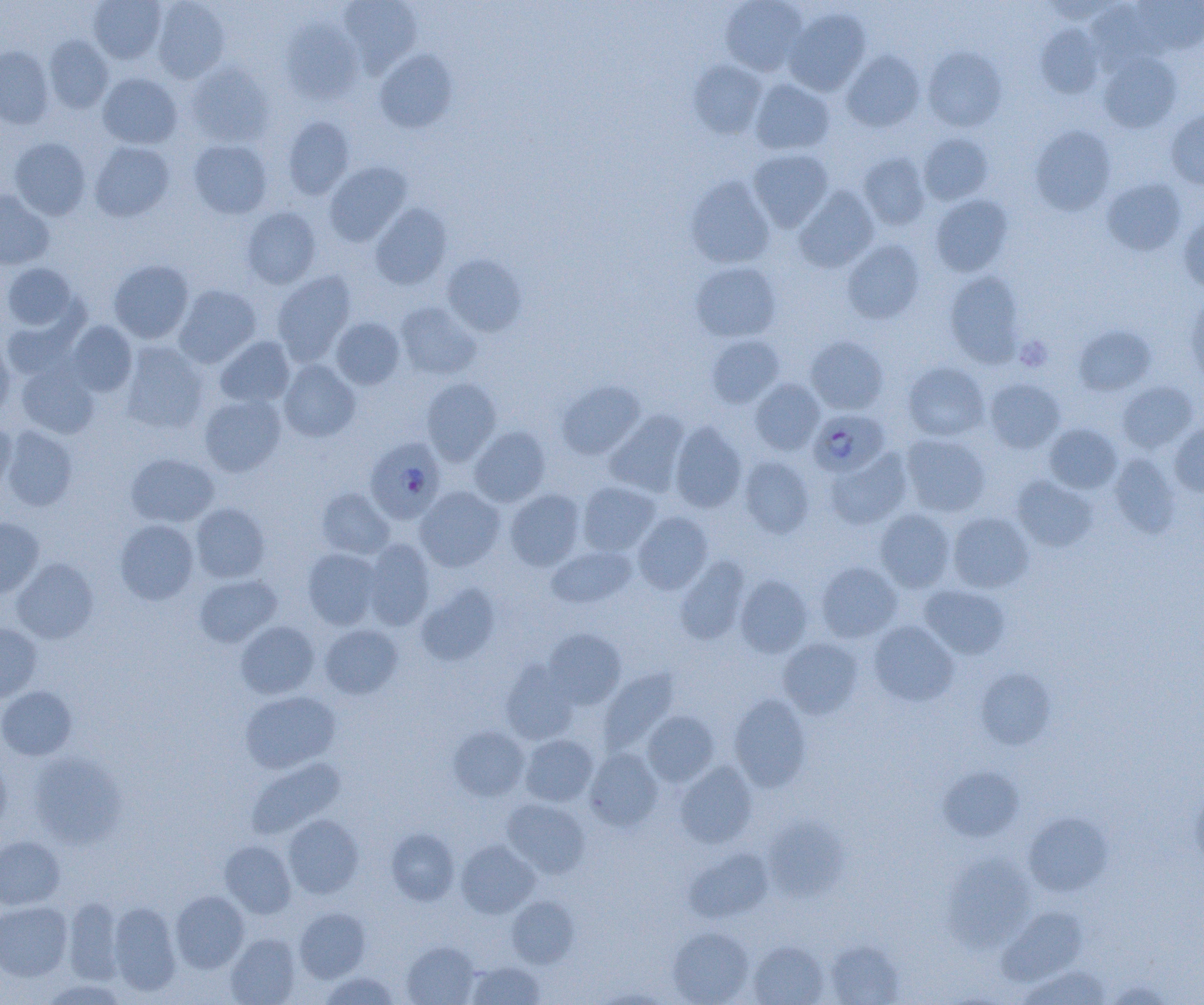 Approximate bounding boxes as named x1/y1/x2/y2 corners in pixels. Platelet locations: (x1=1016, y1=336, x2=1052, y2=371). Uninfected red blood cell locations: (x1=89, y1=0, x2=166, y2=63), (x1=151, y1=0, x2=230, y2=83), (x1=339, y1=0, x2=422, y2=77), (x1=720, y1=0, x2=807, y2=76), (x1=1133, y1=0, x2=1204, y2=55), (x1=1086, y1=2, x2=1162, y2=69), (x1=784, y1=7, x2=870, y2=96), (x1=281, y1=20, x2=363, y2=104), (x1=1036, y1=23, x2=1104, y2=99), (x1=44, y1=36, x2=113, y2=113), (x1=0, y1=46, x2=54, y2=129), (x1=923, y1=46, x2=1007, y2=131), (x1=374, y1=50, x2=458, y2=134), (x1=841, y1=50, x2=925, y2=132), (x1=1099, y1=52, x2=1182, y2=132), (x1=688, y1=59, x2=767, y2=138), (x1=185, y1=62, x2=274, y2=147), (x1=98, y1=72, x2=182, y2=148), (x1=749, y1=78, x2=834, y2=155), (x1=1166, y1=109, x2=1204, y2=190), (x1=282, y1=116, x2=354, y2=199), (x1=1030, y1=125, x2=1116, y2=215), (x1=919, y1=133, x2=994, y2=205), (x1=9, y1=137, x2=91, y2=220), (x1=188, y1=139, x2=273, y2=218), (x1=90, y1=141, x2=174, y2=221), (x1=747, y1=148, x2=834, y2=231), (x1=858, y1=152, x2=930, y2=230), (x1=324, y1=161, x2=412, y2=246), (x1=686, y1=175, x2=775, y2=268), (x1=1102, y1=178, x2=1186, y2=256), (x1=794, y1=186, x2=878, y2=272), (x1=0, y1=190, x2=54, y2=269), (x1=930, y1=194, x2=1013, y2=277), (x1=370, y1=203, x2=451, y2=290), (x1=241, y1=207, x2=321, y2=288), (x1=1178, y1=211, x2=1204, y2=294), (x1=842, y1=239, x2=924, y2=324), (x1=441, y1=254, x2=527, y2=336), (x1=109, y1=259, x2=194, y2=343), (x1=691, y1=261, x2=782, y2=342), (x1=2, y1=262, x2=78, y2=331), (x1=272, y1=270, x2=357, y2=364), (x1=944, y1=271, x2=1025, y2=366), (x1=174, y1=284, x2=261, y2=367), (x1=1184, y1=293, x2=1204, y2=385), (x1=396, y1=301, x2=481, y2=380), (x1=2, y1=308, x2=85, y2=383), (x1=330, y1=317, x2=405, y2=389), (x1=67, y1=320, x2=138, y2=396), (x1=1074, y1=324, x2=1155, y2=396), (x1=706, y1=334, x2=785, y2=408), (x1=805, y1=335, x2=889, y2=414), (x1=215, y1=336, x2=296, y2=408), (x1=0, y1=338, x2=15, y2=419), (x1=120, y1=341, x2=208, y2=434), (x1=278, y1=360, x2=360, y2=442), (x1=903, y1=361, x2=989, y2=442), (x1=16, y1=362, x2=99, y2=439), (x1=421, y1=377, x2=501, y2=465), (x1=984, y1=378, x2=1065, y2=453), (x1=749, y1=379, x2=825, y2=455), (x1=558, y1=380, x2=645, y2=460), (x1=1117, y1=381, x2=1198, y2=453), (x1=198, y1=393, x2=286, y2=477), (x1=604, y1=411, x2=690, y2=497), (x1=0, y1=419, x2=16, y2=493), (x1=669, y1=422, x2=747, y2=513), (x1=1169, y1=422, x2=1204, y2=496), (x1=1044, y1=423, x2=1122, y2=493), (x1=2, y1=426, x2=78, y2=511), (x1=469, y1=426, x2=550, y2=507), (x1=901, y1=434, x2=990, y2=517), (x1=825, y1=448, x2=912, y2=529), (x1=126, y1=453, x2=219, y2=528), (x1=1109, y1=453, x2=1180, y2=537), (x1=739, y1=456, x2=815, y2=538), (x1=1011, y1=475, x2=1097, y2=551), (x1=577, y1=481, x2=660, y2=555), (x1=415, y1=486, x2=505, y2=572), (x1=316, y1=487, x2=394, y2=559), (x1=505, y1=489, x2=585, y2=571), (x1=190, y1=502, x2=270, y2=583), (x1=875, y1=509, x2=956, y2=592), (x1=633, y1=511, x2=713, y2=594), (x1=948, y1=512, x2=1033, y2=593), (x1=0, y1=518, x2=44, y2=597), (x1=115, y1=519, x2=199, y2=604), (x1=363, y1=539, x2=435, y2=630), (x1=546, y1=544, x2=637, y2=608), (x1=303, y1=548, x2=382, y2=629), (x1=675, y1=556, x2=750, y2=645), (x1=11, y1=558, x2=98, y2=643), (x1=816, y1=562, x2=902, y2=643), (x1=195, y1=574, x2=281, y2=647), (x1=735, y1=574, x2=812, y2=657), (x1=416, y1=582, x2=500, y2=666), (x1=919, y1=584, x2=1011, y2=659), (x1=868, y1=620, x2=959, y2=706), (x1=236, y1=621, x2=320, y2=699), (x1=0, y1=623, x2=42, y2=702), (x1=320, y1=624, x2=402, y2=699), (x1=543, y1=629, x2=626, y2=709), (x1=778, y1=638, x2=863, y2=718), (x1=501, y1=660, x2=578, y2=744), (x1=599, y1=667, x2=680, y2=754), (x1=975, y1=667, x2=1055, y2=749), (x1=0, y1=685, x2=77, y2=760), (x1=240, y1=691, x2=340, y2=774), (x1=729, y1=694, x2=811, y2=791), (x1=642, y1=710, x2=720, y2=787), (x1=448, y1=725, x2=530, y2=801), (x1=520, y1=734, x2=598, y2=806), (x1=584, y1=749, x2=663, y2=830), (x1=28, y1=752, x2=127, y2=847), (x1=0, y1=753, x2=12, y2=834), (x1=246, y1=757, x2=345, y2=839), (x1=675, y1=762, x2=757, y2=848), (x1=938, y1=766, x2=1024, y2=842), (x1=1191, y1=786, x2=1204, y2=869), (x1=502, y1=799, x2=590, y2=878), (x1=1023, y1=812, x2=1113, y2=896), (x1=282, y1=814, x2=363, y2=898), (x1=763, y1=818, x2=847, y2=900), (x1=386, y1=828, x2=460, y2=906), (x1=0, y1=836, x2=65, y2=910), (x1=220, y1=840, x2=296, y2=918), (x1=456, y1=840, x2=540, y2=917), (x1=684, y1=847, x2=773, y2=922), (x1=943, y1=853, x2=1035, y2=950), (x1=171, y1=890, x2=249, y2=973), (x1=507, y1=896, x2=579, y2=968), (x1=64, y1=897, x2=126, y2=984), (x1=0, y1=900, x2=73, y2=981), (x1=108, y1=902, x2=181, y2=996), (x1=294, y1=907, x2=370, y2=982), (x1=999, y1=907, x2=1087, y2=985), (x1=667, y1=926, x2=753, y2=1005), (x1=225, y1=933, x2=300, y2=1005), (x1=401, y1=940, x2=480, y2=1005), (x1=825, y1=940, x2=904, y2=1004), (x1=748, y1=941, x2=828, y2=1005), (x1=466, y1=960, x2=546, y2=1005), (x1=1017, y1=965, x2=1112, y2=1005), (x1=318, y1=972, x2=399, y2=1004), (x1=38, y1=978, x2=129, y2=1005), (x1=1103, y1=979, x2=1176, y2=1004). Plasmodium falciparum-infected red blood cell locations: (x1=809, y1=409, x2=889, y2=477), (x1=364, y1=436, x2=444, y2=523). Slide-level diagnosis: Plasmodium falciparum. Optical microscopy. One field of a larger specimen. Thin blood film. Image is 1204×1005 pixels. 1000x magnification.